State the blood parasite species.
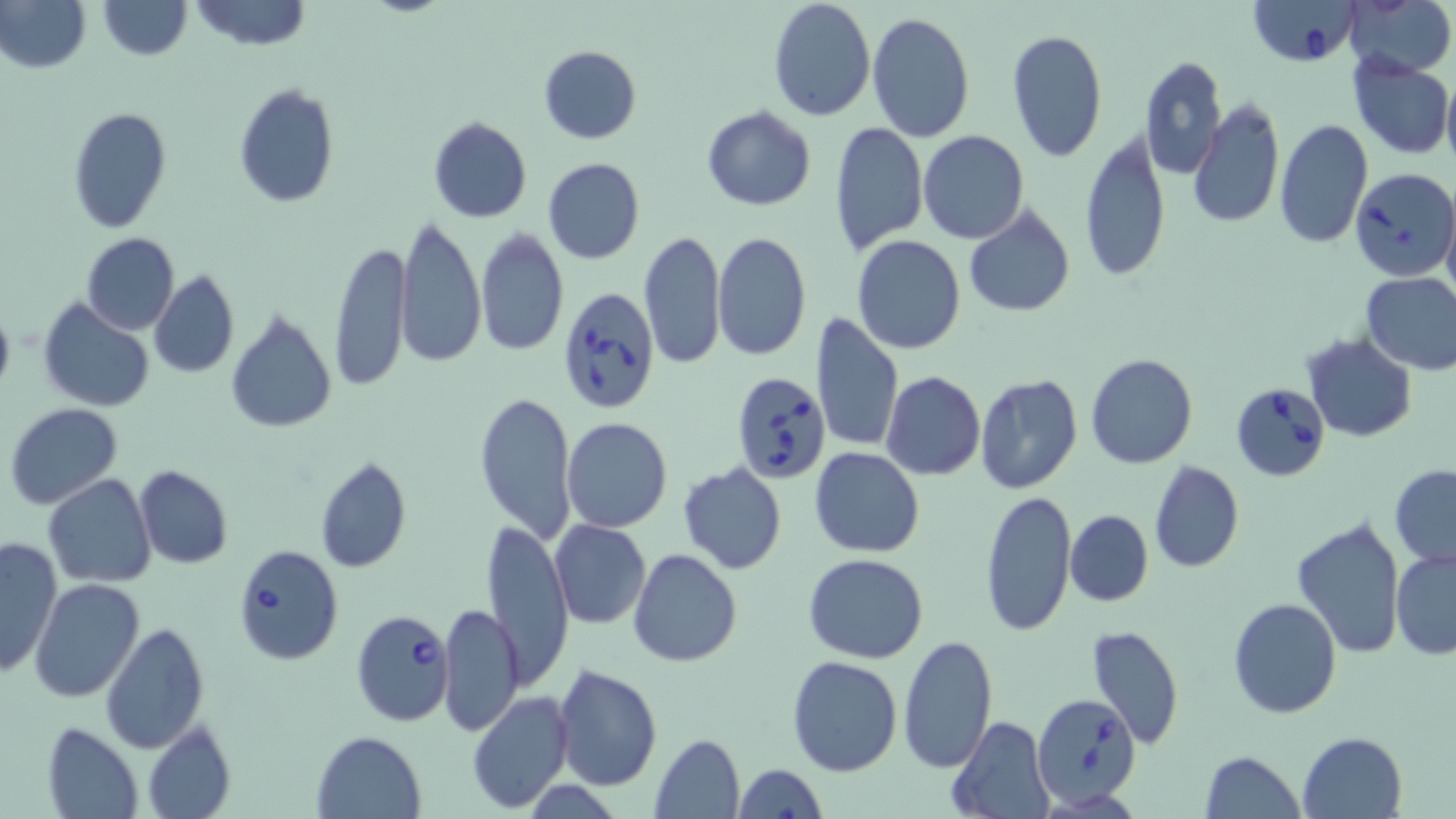
Babesia divergens.

{
  "magnification": "1000x",
  "babesia_divergens_infected_red_blood_cell_locations": "approximate bounding boxes as named x1/y1/x2/y2 corners in pixels: (x1=1246, y1=0, x2=1364, y2=68), (x1=1350, y1=167, x2=1455, y2=281), (x1=560, y1=287, x2=662, y2=414), (x1=735, y1=369, x2=835, y2=484), (x1=1230, y1=379, x2=1331, y2=481), (x1=233, y1=546, x2=342, y2=664), (x1=355, y1=610, x2=455, y2=724), (x1=1031, y1=692, x2=1141, y2=809)",
  "uninfected_red_blood_cell_locations": "approximate bounding boxes as named x1/y1/x2/y2 corners in pixels: (x1=1, y1=0, x2=89, y2=73), (x1=97, y1=0, x2=192, y2=60), (x1=189, y1=0, x2=313, y2=50), (x1=767, y1=0, x2=876, y2=123), (x1=1343, y1=0, x2=1454, y2=77), (x1=866, y1=11, x2=974, y2=142), (x1=1005, y1=29, x2=1109, y2=163), (x1=538, y1=45, x2=641, y2=144), (x1=1347, y1=53, x2=1454, y2=160), (x1=1139, y1=55, x2=1227, y2=178), (x1=1441, y1=75, x2=1456, y2=178), (x1=233, y1=83, x2=338, y2=209), (x1=1188, y1=98, x2=1284, y2=230), (x1=65, y1=106, x2=171, y2=233), (x1=703, y1=107, x2=816, y2=211), (x1=428, y1=117, x2=531, y2=223), (x1=1275, y1=118, x2=1372, y2=249), (x1=829, y1=121, x2=927, y2=257), (x1=918, y1=130, x2=1028, y2=244), (x1=1080, y1=130, x2=1171, y2=286), (x1=542, y1=157, x2=644, y2=264), (x1=1442, y1=199, x2=1456, y2=303), (x1=964, y1=204, x2=1076, y2=319), (x1=396, y1=215, x2=485, y2=370), (x1=476, y1=227, x2=568, y2=357), (x1=639, y1=230, x2=725, y2=370), (x1=712, y1=231, x2=810, y2=362), (x1=81, y1=232, x2=180, y2=335), (x1=851, y1=236, x2=966, y2=355), (x1=330, y1=239, x2=411, y2=395), (x1=148, y1=269, x2=239, y2=378), (x1=1359, y1=270, x2=1456, y2=376), (x1=37, y1=299, x2=155, y2=412), (x1=0, y1=301, x2=16, y2=404), (x1=224, y1=310, x2=337, y2=433), (x1=811, y1=313, x2=905, y2=454), (x1=1301, y1=334, x2=1418, y2=442), (x1=1084, y1=353, x2=1199, y2=469), (x1=881, y1=370, x2=985, y2=479), (x1=974, y1=374, x2=1083, y2=494), (x1=473, y1=389, x2=577, y2=544), (x1=5, y1=403, x2=123, y2=508), (x1=560, y1=418, x2=671, y2=534), (x1=809, y1=448, x2=926, y2=558), (x1=313, y1=455, x2=412, y2=574), (x1=1149, y1=460, x2=1242, y2=573), (x1=679, y1=461, x2=788, y2=574), (x1=1389, y1=464, x2=1456, y2=566), (x1=133, y1=465, x2=234, y2=570), (x1=44, y1=474, x2=158, y2=588), (x1=979, y1=490, x2=1077, y2=636), (x1=1065, y1=510, x2=1153, y2=606), (x1=1292, y1=516, x2=1408, y2=657), (x1=481, y1=517, x2=573, y2=688), (x1=550, y1=520, x2=652, y2=630), (x1=0, y1=534, x2=62, y2=678), (x1=629, y1=548, x2=742, y2=666), (x1=1390, y1=548, x2=1456, y2=660), (x1=803, y1=553, x2=929, y2=663), (x1=28, y1=577, x2=145, y2=703), (x1=1228, y1=598, x2=1341, y2=718), (x1=437, y1=603, x2=525, y2=737), (x1=100, y1=623, x2=211, y2=752), (x1=1084, y1=624, x2=1183, y2=751), (x1=896, y1=635, x2=999, y2=774), (x1=787, y1=655, x2=902, y2=775), (x1=552, y1=663, x2=662, y2=792), (x1=466, y1=691, x2=574, y2=810), (x1=946, y1=715, x2=1052, y2=819), (x1=142, y1=719, x2=236, y2=819), (x1=41, y1=721, x2=145, y2=819), (x1=313, y1=730, x2=428, y2=818), (x1=1297, y1=731, x2=1407, y2=819), (x1=648, y1=734, x2=746, y2=819), (x1=1198, y1=750, x2=1306, y2=819), (x1=732, y1=763, x2=827, y2=819)",
  "stain": "May-Grünwald-Giemsa",
  "field_of_view": "one of a larger specimen",
  "modality": "light microscopy",
  "preparation": "thin blood smear",
  "image_size": "1456×819 pixels"
}